Report the malaria status of this cell.
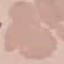
Uninfected.

{
  "image_type": "automatically extracted cell patch, resized to 64 × 64 pixels",
  "preparation": "thin blood smear",
  "stain": "Giemsa",
  "capture": "smartphone camera at the microscope eyepiece"
}